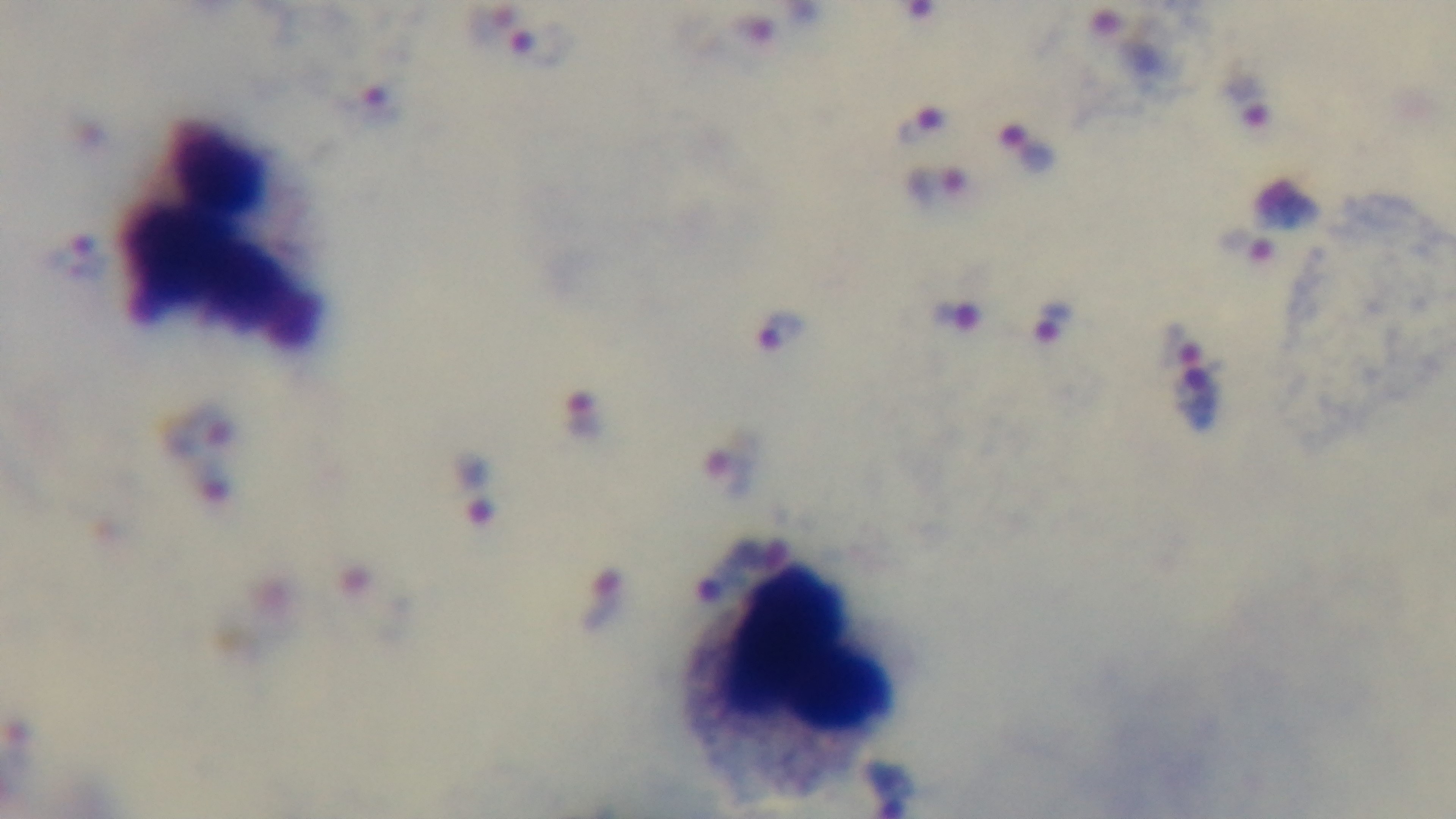 Malaria status: positive. Oil-immersion objective, 100x. Preparation: thick blood film. Captured with a mounted 4K digital camera. Photomicrograph. Giemsa-stained. One field from the slide.